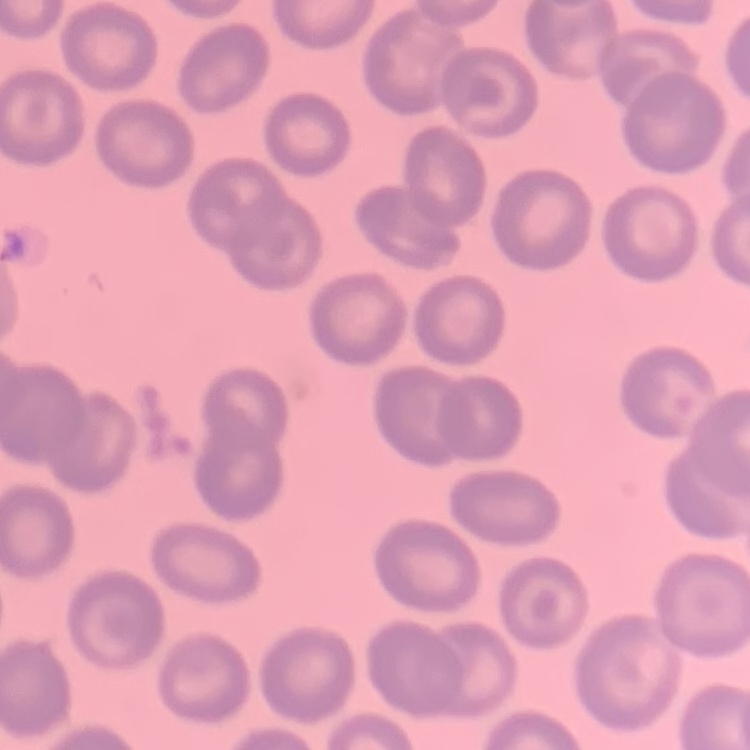 The erythrocytes exhibit no rouleaux formation. Stained with either Field's or Giemsa. Square crop of a larger photomicrograph. Thin peripheral smear.